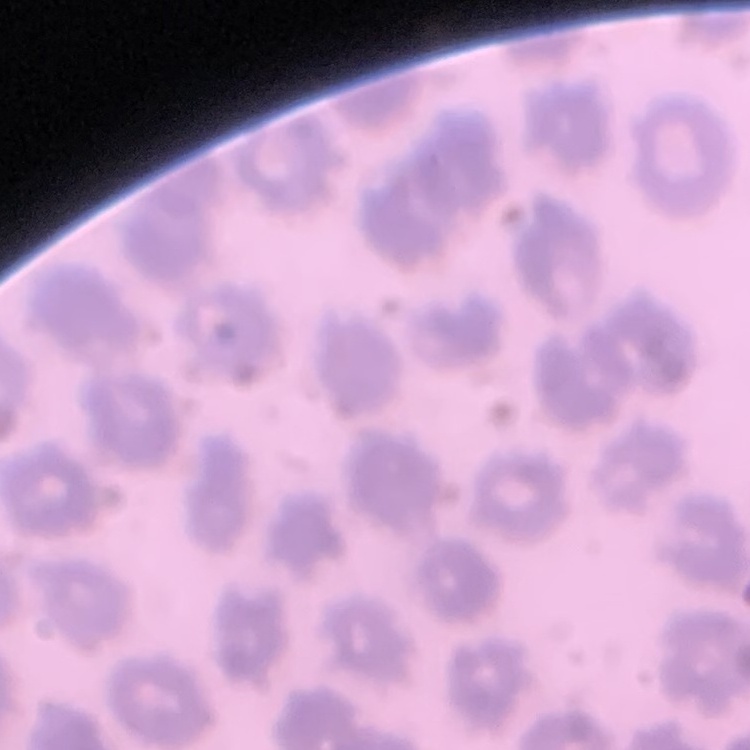 The red blood cells exhibit no rouleaux formation. Field's or Giemsa stain. Thin blood smear. Square crop of a larger photomicrograph.